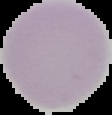 Image is 112×115 pixels. Result: no malaria parasites detected. From a thin blood smear. The area outside the segmented cell region is set to black.